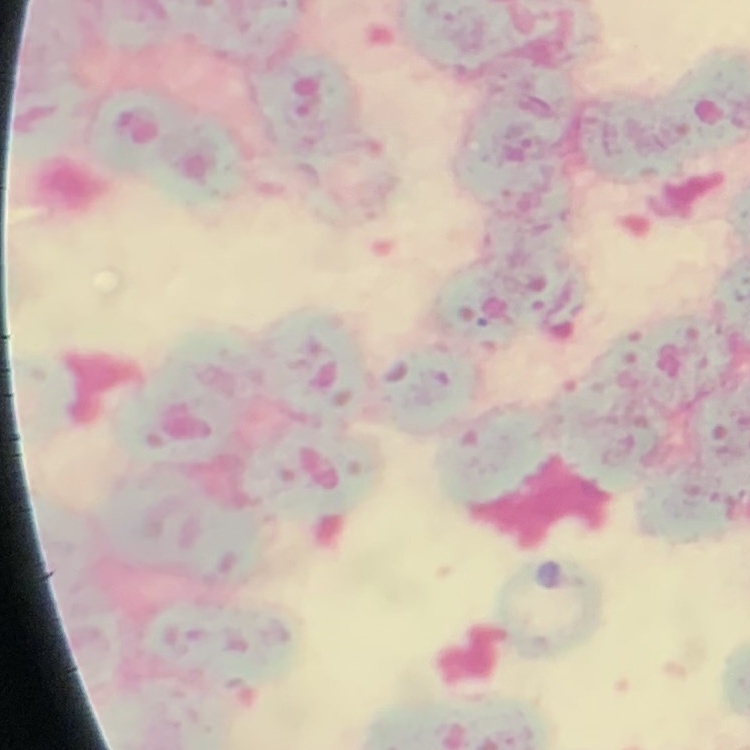 The red blood cells exhibit rouleaux formation. Thin peripheral smear. Square crop of a larger photomicrograph. Stained with either Field's or Giemsa.